Describe the morphology of the red blood cells.
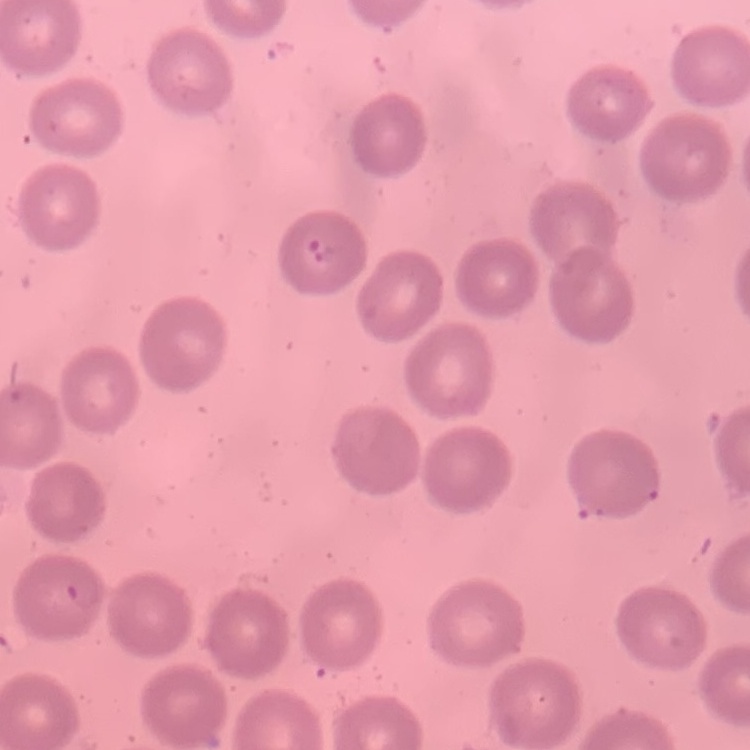
No rouleaux formation.

Summary:
  - Preparation: thin blood film
  - Stain: Field's or Giemsa
  - Image type: one tile cut from a larger photomicrograph